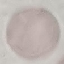
Summary:
  - Result: no malaria parasites detected
  - Preparation: thin smear
  - Image type: cell patch, automatically extracted from a larger field of view and resized to 64 × 64 pixels
  - Capture: smartphone through the microscope eyepiece
  - Stain: Giemsa